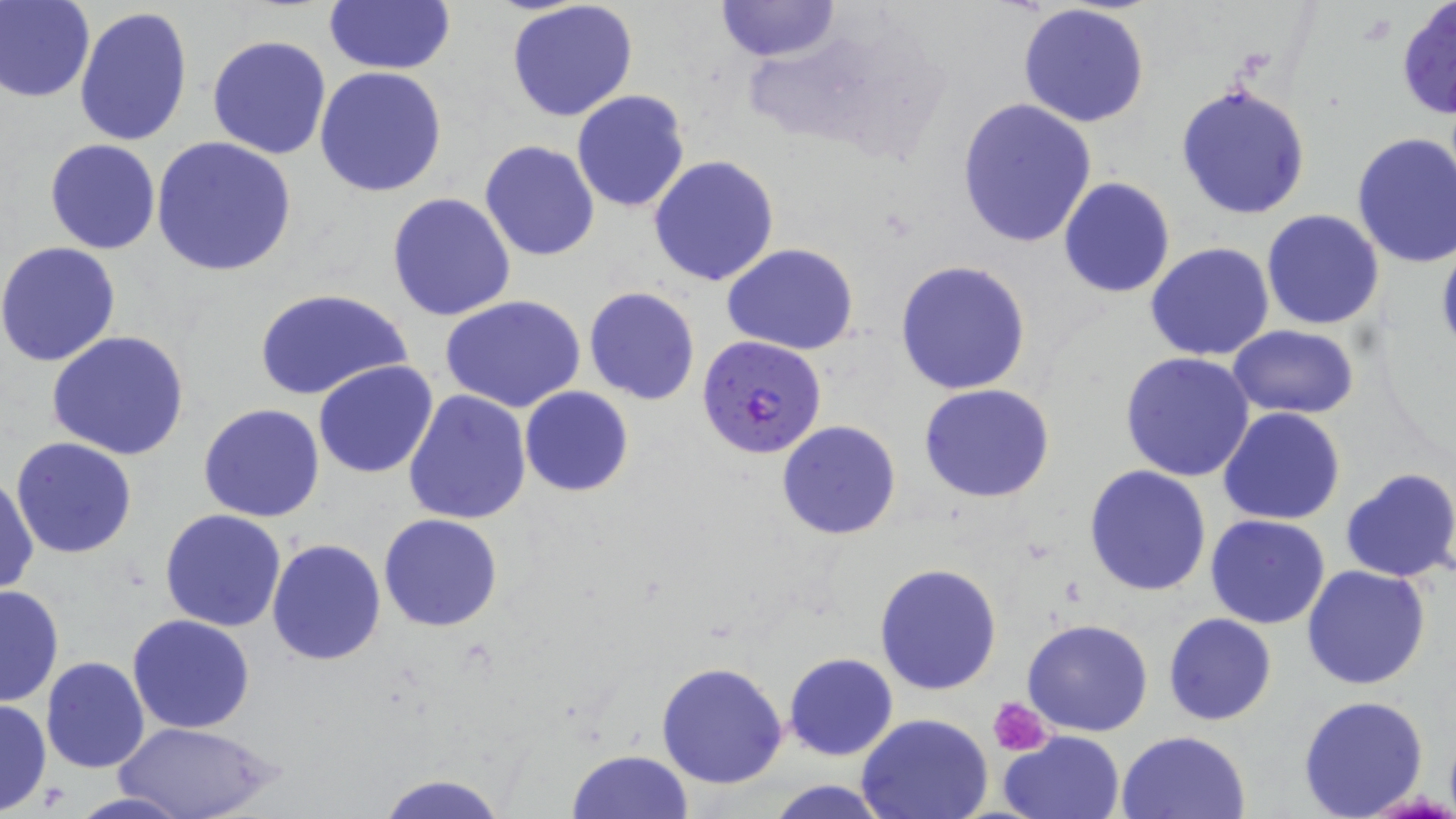
Summary:
  - Coordinate format: approximate bounding boxes as named x1/y1/x2/y2 corners in pixels
  - Uninfected red blood cell locations: (x1=1, y1=0, x2=94, y2=103), (x1=322, y1=0, x2=458, y2=75), (x1=506, y1=0, x2=639, y2=121), (x1=715, y1=0, x2=840, y2=64), (x1=1396, y1=1, x2=1456, y2=120), (x1=1017, y1=4, x2=1151, y2=129), (x1=74, y1=6, x2=192, y2=147), (x1=207, y1=34, x2=332, y2=159), (x1=315, y1=66, x2=448, y2=197), (x1=1176, y1=82, x2=1311, y2=219), (x1=570, y1=90, x2=690, y2=212), (x1=957, y1=98, x2=1097, y2=248), (x1=1351, y1=131, x2=1456, y2=270), (x1=150, y1=136, x2=299, y2=277), (x1=46, y1=139, x2=161, y2=255), (x1=479, y1=140, x2=600, y2=261), (x1=649, y1=154, x2=780, y2=287), (x1=1058, y1=177, x2=1176, y2=298), (x1=387, y1=193, x2=517, y2=321), (x1=1261, y1=209, x2=1384, y2=329), (x1=1435, y1=237, x2=1456, y2=361), (x1=0, y1=242, x2=122, y2=368), (x1=722, y1=243, x2=860, y2=353), (x1=1145, y1=243, x2=1275, y2=362), (x1=895, y1=259, x2=1032, y2=396), (x1=583, y1=286, x2=701, y2=405), (x1=256, y1=287, x2=412, y2=403), (x1=440, y1=294, x2=586, y2=413), (x1=1227, y1=325, x2=1358, y2=418), (x1=46, y1=331, x2=191, y2=462), (x1=1121, y1=351, x2=1256, y2=481), (x1=313, y1=360, x2=438, y2=478), (x1=918, y1=382, x2=1055, y2=503), (x1=519, y1=386, x2=633, y2=497), (x1=402, y1=389, x2=531, y2=525), (x1=199, y1=403, x2=326, y2=522), (x1=1219, y1=408, x2=1347, y2=527), (x1=776, y1=419, x2=901, y2=541), (x1=11, y1=437, x2=138, y2=558), (x1=1084, y1=464, x2=1213, y2=595), (x1=1339, y1=467, x2=1456, y2=583), (x1=0, y1=472, x2=38, y2=597), (x1=160, y1=509, x2=288, y2=631), (x1=378, y1=513, x2=504, y2=632), (x1=1205, y1=514, x2=1331, y2=628), (x1=266, y1=537, x2=385, y2=666), (x1=874, y1=563, x2=1002, y2=695), (x1=1300, y1=563, x2=1432, y2=690), (x1=0, y1=584, x2=65, y2=708), (x1=127, y1=613, x2=256, y2=734), (x1=1163, y1=613, x2=1277, y2=725), (x1=1021, y1=619, x2=1152, y2=737), (x1=784, y1=652, x2=898, y2=761), (x1=41, y1=656, x2=149, y2=775), (x1=656, y1=661, x2=789, y2=789), (x1=1298, y1=694, x2=1431, y2=818), (x1=0, y1=698, x2=51, y2=815), (x1=857, y1=714, x2=992, y2=819), (x1=118, y1=719, x2=278, y2=819), (x1=1116, y1=729, x2=1251, y2=818), (x1=1000, y1=730, x2=1126, y2=819), (x1=567, y1=748, x2=694, y2=819), (x1=375, y1=771, x2=510, y2=818), (x1=764, y1=780, x2=893, y2=818), (x1=63, y1=792, x2=195, y2=819)
  - Platelet locations: (x1=990, y1=697, x2=1053, y2=757)
  - Plasmodium falciparum-infected red blood cell locations: (x1=696, y1=334, x2=825, y2=460)
  - Slide-level diagnosis: Plasmodium falciparum
  - Preparation: thin blood film
  - Image size: 1456×819 pixels
  - Field of view: single
  - Stain: May-Grünwald-Giemsa
  - Magnification: 1000x
  - Modality: optical microscopy